Locate every WBC.
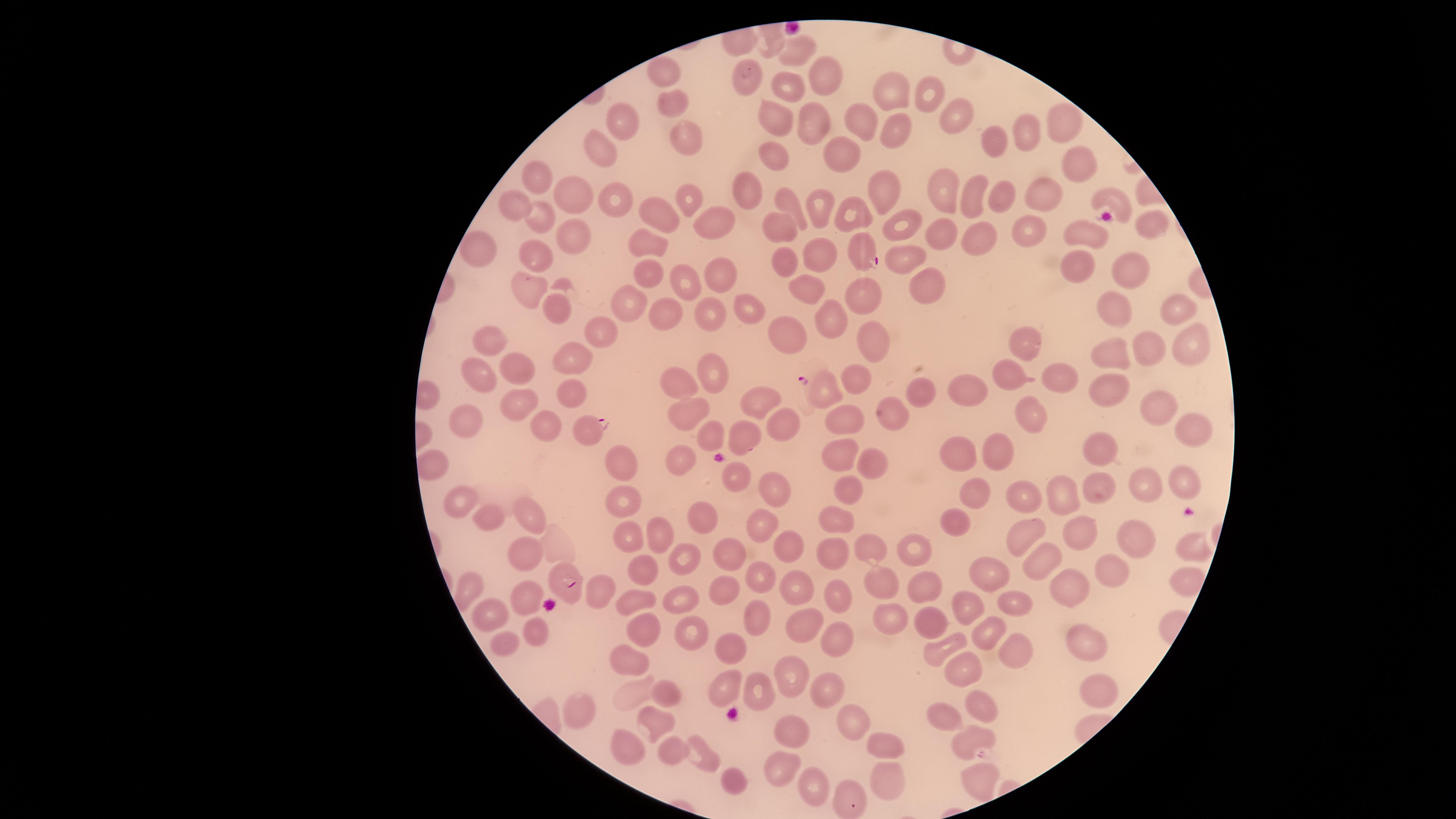

No WBCs identified.

Approximate marker points as {x, y} in pixels.
Summary:
  - Uninfected RBCs: {798, 50}, {666, 73}, {746, 78}, {821, 79}, {786, 86}, {897, 88}, {930, 100}, {677, 103}, {774, 117}, {853, 120}, {806, 121}, {622, 122}, {960, 122}, {1067, 126}, {899, 134}, {684, 137}, {1031, 137}, {999, 144}, {602, 150}, {848, 151}, {777, 157}, {1078, 163}, {538, 173}, {748, 191}, {575, 193}, {940, 193}, {970, 195}, {615, 196}, {688, 196}, {1004, 196}, {889, 197}, {1045, 200}, {1113, 200}, {786, 203}, {513, 204}, {815, 208}, {660, 216}, {854, 217}, {541, 218}, {716, 218}, {1152, 220}, {895, 225}, {1093, 230}, {1037, 232}, {788, 233}, {936, 233}, {570, 235}, {984, 237}, {648, 245}, {477, 249}, {822, 255}, {899, 256}, {539, 258}, {1076, 259}, {784, 268}, {1127, 268}, {649, 272}, {720, 272}, {685, 280}, {927, 281}, {524, 283}, {801, 287}, {865, 296}, {546, 303}, {628, 303}, {743, 304}, {1175, 307}, {713, 309}, {655, 310}, {1113, 312}, {829, 315}, {598, 329}, {784, 335}, {869, 336}, {494, 339}, {1187, 345}, {1025, 348}, {1152, 351}, {570, 358}, {1112, 359}, {520, 369}, {711, 371}, {479, 373}, {1005, 375}, {859, 377}, {1063, 379}, {1109, 386}, {965, 388}, {570, 392}, {921, 392}, {682, 394}, {1155, 395}, {827, 397}, {757, 400}, {520, 401}, {682, 416}, {1033, 418}, {468, 419}, {849, 421}, {544, 423}, {781, 424}, {1192, 425}, {744, 433}, {711, 436}, {1101, 450}, {998, 455}, {960, 456}, {837, 458}, {681, 463}, {870, 464}, {619, 467}, {734, 477}, {1184, 481}, {768, 489}, {849, 491}, {1091, 491}, {1146, 492}, {979, 493}, {463, 497}, {1063, 497}, {1026, 500}, {617, 502}, {533, 514}, {829, 515}, {488, 518}, {699, 518}, {952, 522}, {763, 524}, {1083, 531}, {1024, 532}, {662, 537}, {625, 539}, {1137, 540}, {557, 542}, {1190, 544}, {782, 545}, {914, 545}, {868, 547}, {833, 551}, {530, 555}, {731, 555}, {686, 559}, {1030, 559}, {644, 572}, {988, 572}, {1111, 573}, {758, 576}, {1180, 580}, {798, 582}, {877, 583}, {1068, 584}, {925, 585}, {471, 588}, {596, 588}, {526, 593}, {729, 593}, {835, 593}, {675, 598}, {630, 601}, {1012, 604}, {967, 610}, {496, 611}, {756, 614}, {887, 618}, {930, 620}, {802, 625}, {644, 627}, {684, 630}, {536, 633}, {985, 633}, {839, 639}, {501, 643}, {1085, 644}, {723, 649}, {936, 649}, {1013, 653}, {629, 660}, {963, 666}, {789, 675}, {1100, 688}, {721, 689}, {660, 690}, {824, 694}, {758, 695}, {630, 697}, {979, 702}, {582, 710}, {948, 718}, {653, 719}, {844, 719}, {790, 727}, {971, 738}, {624, 745}, {884, 749}, {668, 754}, {703, 761}, {778, 764}, {976, 777}, {734, 780}, {885, 783}, {813, 786}, {845, 795}
  - Parasitized RBCs: {862, 256}, {589, 429}, {568, 584}
  - Presence: malaria parasites detected
  - Visible region: circular
  - Preparation: thin smear of blood
  - Field of view: single
  - Image size: 1456×819 pixels
  - Capture: smartphone photograph through the microscope eyepiece
  - Species: Plasmodium falciparum
  - Stain: Giemsa